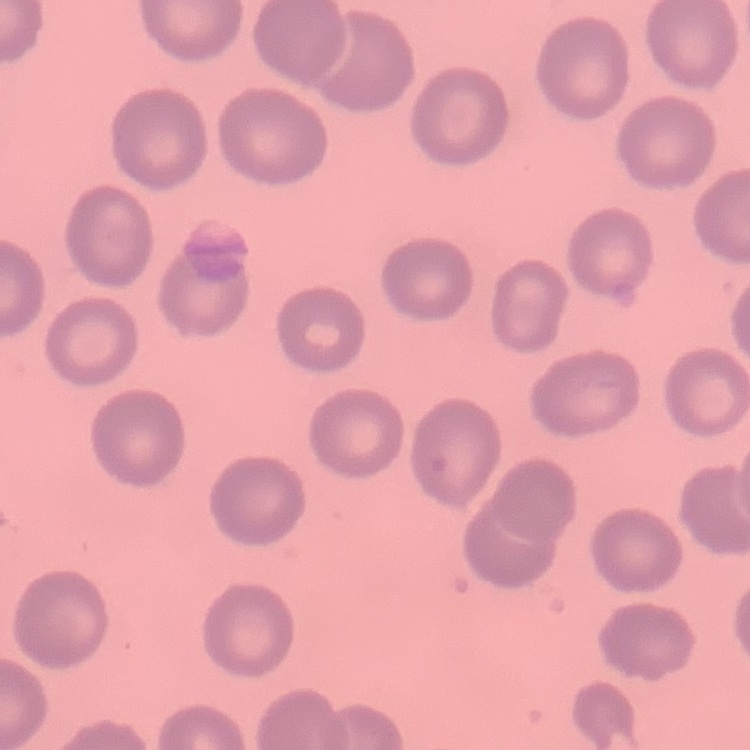
Summary:
  - Erythrocyte morphology: no rouleaux formation
  - Preparation: thin peripheral smear
  - Image type: square crop of a larger photomicrograph
  - Stain: Field's or Giemsa